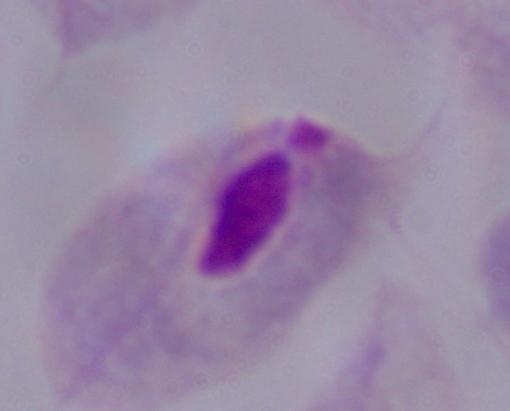 A trichomonad is shown. Captured at 1000x magnification. Micrograph.